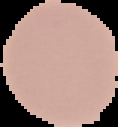
Summary:
  - Image size: 118×127 pixels
  - Preparation: thin blood film
  - Image type: segmented cell region on a black background
  - Malaria status: uninfected